Name the blood parasite species.
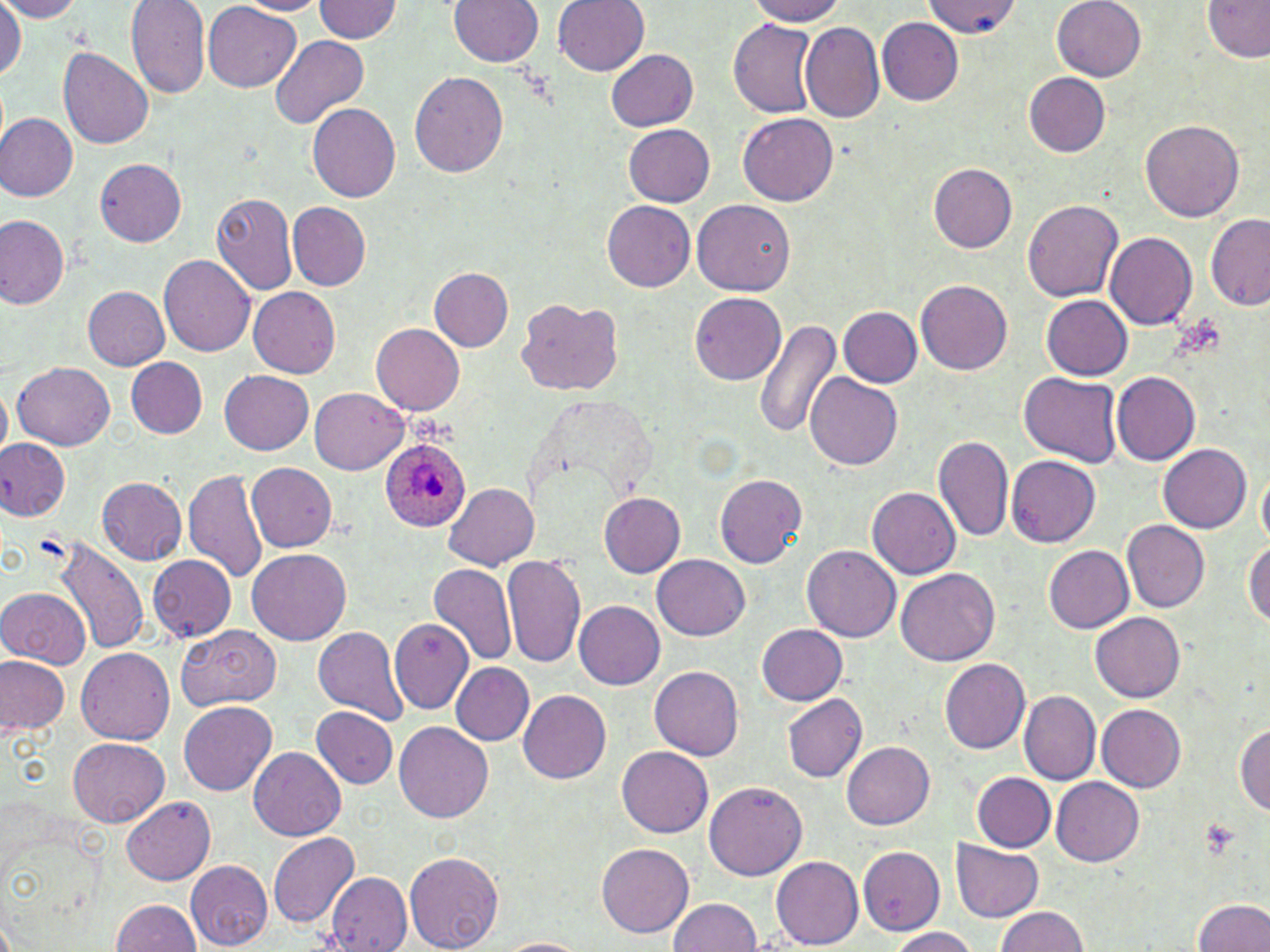
Plasmodium ovale.

Approximate bounding boxes as [x1, y1, x2, y2] in pixels. Platelet locations: [1194, 818, 1241, 862]. Plasmodium ovale-infected red blood cell locations: [378, 438, 469, 532]. Uninfected red blood cell locations: [0, 0, 86, 22], [233, 0, 329, 16], [449, 0, 543, 65], [554, 0, 650, 75], [749, 0, 848, 25], [313, 1, 404, 44], [925, 1, 1017, 38], [1053, 1, 1146, 81], [1202, 1, 1270, 61], [0, 2, 25, 82], [126, 2, 211, 101], [204, 4, 301, 91], [877, 17, 964, 105], [727, 19, 822, 118], [799, 22, 885, 123], [270, 34, 369, 130], [58, 47, 154, 151], [606, 49, 699, 130], [409, 71, 508, 177], [1025, 73, 1111, 156], [307, 103, 401, 202], [0, 112, 78, 200], [738, 113, 837, 204], [1141, 120, 1244, 221], [624, 125, 716, 206], [95, 158, 186, 245], [928, 164, 1017, 252], [212, 192, 298, 295], [1022, 197, 1123, 301], [693, 199, 794, 296], [601, 200, 696, 292], [288, 203, 370, 290], [1205, 212, 1270, 310], [0, 215, 70, 308], [1105, 231, 1198, 330], [159, 254, 257, 357], [430, 268, 513, 350], [916, 279, 1011, 374], [247, 285, 340, 377], [82, 286, 171, 370], [690, 293, 785, 385], [1043, 296, 1133, 380], [514, 299, 624, 396], [838, 305, 922, 387], [755, 319, 842, 441], [371, 324, 464, 415], [125, 357, 208, 438], [13, 360, 115, 451], [1111, 370, 1201, 465], [219, 371, 313, 454], [1021, 372, 1123, 466], [805, 374, 903, 469], [0, 381, 11, 465], [310, 388, 408, 474], [934, 434, 1013, 541], [0, 439, 69, 522], [1157, 443, 1251, 533], [1006, 456, 1101, 547], [246, 463, 337, 551], [1257, 463, 1270, 548], [184, 468, 271, 583], [714, 473, 808, 567], [96, 476, 186, 564], [445, 483, 538, 569], [867, 487, 962, 579], [598, 492, 685, 577], [1122, 521, 1210, 612], [54, 535, 148, 657], [1243, 538, 1270, 627], [802, 545, 900, 642], [1043, 545, 1135, 632], [248, 549, 349, 646], [502, 551, 587, 670], [148, 555, 236, 641], [653, 555, 749, 641], [429, 563, 517, 665], [895, 566, 999, 664], [2, 589, 90, 667], [574, 600, 666, 689], [1091, 612, 1185, 703], [390, 617, 473, 714], [756, 623, 848, 704], [175, 624, 282, 709], [312, 626, 408, 725], [76, 647, 174, 744], [0, 656, 69, 738], [940, 658, 1032, 753], [452, 663, 533, 745], [650, 666, 744, 759], [1019, 689, 1101, 785], [519, 690, 611, 783], [781, 694, 867, 782], [179, 701, 277, 797], [1097, 704, 1186, 791], [312, 706, 398, 789], [393, 722, 493, 822], [1233, 723, 1270, 814], [68, 738, 171, 828], [840, 741, 935, 829], [249, 746, 345, 840], [617, 746, 713, 837], [972, 773, 1055, 851], [1051, 777, 1145, 865], [704, 781, 806, 879], [121, 795, 215, 885], [268, 832, 358, 927], [951, 841, 1044, 921], [596, 843, 694, 937], [858, 846, 944, 933], [404, 848, 503, 952], [771, 853, 863, 949], [185, 859, 272, 950], [326, 872, 412, 951], [1194, 896, 1270, 952], [110, 898, 200, 952], [670, 899, 763, 952], [995, 906, 1088, 952], [887, 927, 979, 952], [497, 938, 589, 952]. Image is 1270×952 pixels. Thin blood film. Optical microscopy. One field of a larger specimen. May-Grünwald-Giemsa-stained preparation. Captured at 1000x magnification.